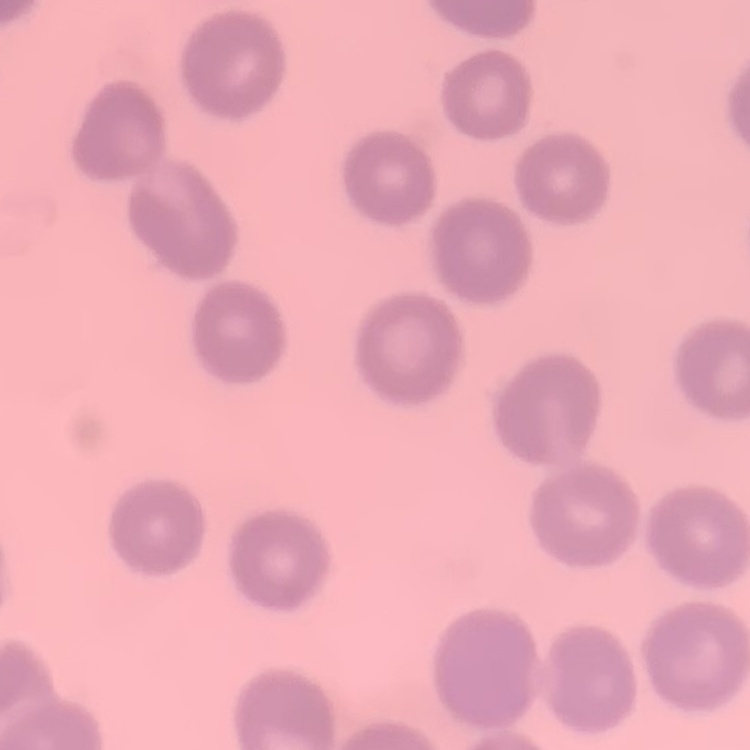
{
  "red_blood_cell_morphology": "no rouleaux formation",
  "image_type": "one tile cut from a larger photomicrograph",
  "preparation": "thin blood film",
  "stain": "Field's or Giemsa"
}